Assess this cell for malaria.
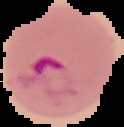
It is parasitized.

preparation = thin blood smear
image type = segmented cell region with the area outside set to black
image size = 124×127 pixels